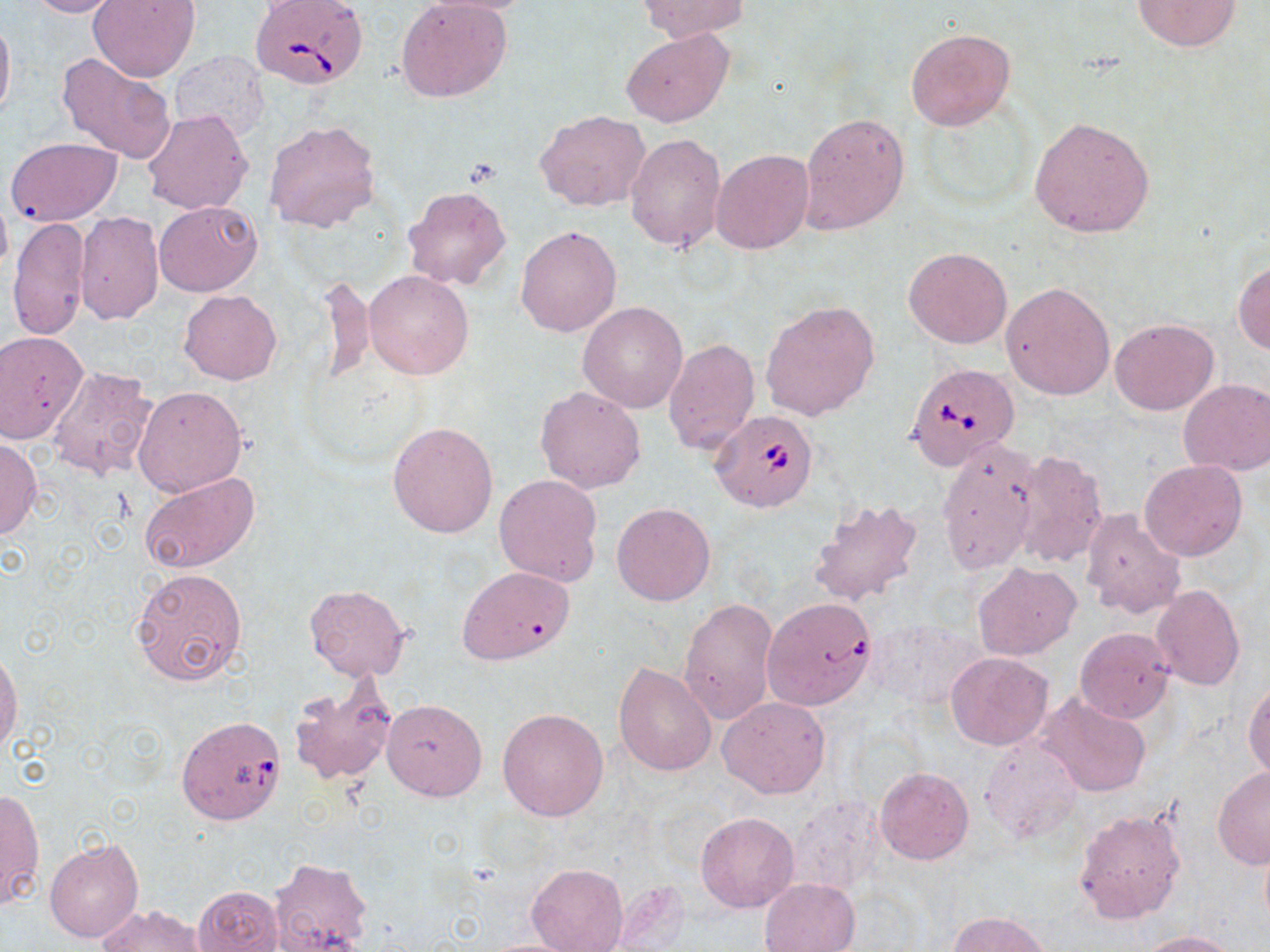

slide_level_diagnosis: Babesia divergens
preparation: thin blood film
modality: light microscopy
magnification: 1000x
field_of_view: single
stain: May-Grünwald-Giemsa
uninfected_red_blood_cell_locations: 'approximate bounding boxes as [x1, y1, x2, y2] in pixels: [24, 0, 123, 18], [89, 0, 201, 81], [397, 0, 512, 103], [417, 0, 551, 15], [636, 0, 750, 40], [1131, 0, 1242, 52], [0, 11, 15, 126], [905, 27, 1015, 130], [621, 28, 733, 126], [57, 52, 177, 165], [168, 52, 269, 141], [142, 108, 254, 216], [536, 111, 652, 213], [798, 113, 910, 234], [1029, 117, 1155, 237], [263, 119, 382, 235], [625, 134, 726, 253], [5, 137, 122, 226], [711, 149, 813, 254], [401, 185, 511, 290], [0, 190, 12, 282], [155, 201, 261, 297], [73, 211, 163, 324], [8, 216, 92, 342], [515, 226, 621, 337], [903, 247, 1012, 349], [1233, 257, 1270, 354], [364, 270, 474, 380], [320, 272, 376, 391], [1001, 282, 1114, 401], [180, 290, 281, 384], [760, 299, 880, 420], [578, 302, 687, 412], [1109, 317, 1219, 416], [0, 332, 86, 443], [664, 338, 760, 457], [47, 366, 158, 481], [1179, 378, 1270, 476], [133, 385, 245, 497], [535, 386, 646, 494], [387, 421, 498, 538], [0, 437, 42, 539], [936, 439, 1040, 574], [1011, 450, 1107, 568], [1139, 459, 1248, 560], [138, 470, 260, 574], [494, 474, 604, 586], [808, 496, 924, 608], [612, 503, 715, 605], [1080, 508, 1185, 620], [972, 562, 1080, 661], [455, 565, 575, 665], [130, 567, 248, 688], [305, 583, 412, 680], [1150, 585, 1246, 692], [677, 596, 778, 724], [869, 617, 988, 711], [1075, 627, 1173, 723], [0, 650, 21, 757], [947, 652, 1052, 750], [613, 660, 716, 777], [287, 677, 398, 786], [1244, 679, 1270, 781], [1039, 692, 1152, 798], [718, 697, 830, 798], [382, 699, 488, 800], [498, 707, 608, 820], [978, 734, 1082, 841], [875, 767, 973, 865], [1212, 768, 1270, 870], [0, 789, 44, 912], [781, 793, 886, 896], [1073, 808, 1185, 926], [696, 811, 799, 912], [45, 840, 143, 943], [268, 858, 371, 950], [526, 863, 628, 951], [759, 878, 859, 952], [192, 885, 284, 952], [98, 904, 207, 951], [948, 910, 1053, 952], [1134, 930, 1239, 951]'
babesia_divergens_infected_red_blood_cell_locations: 'approximate bounding boxes as [x1, y1, x2, y2] in pixels: [248, 0, 369, 87], [910, 367, 1023, 472], [709, 411, 818, 513], [765, 603, 875, 710], [178, 717, 290, 827]'
image_size: 1270×952 pixels